Name the cell type shown.
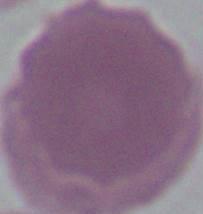
This is an erythrocyte.

1000x magnification. Photomicrograph.